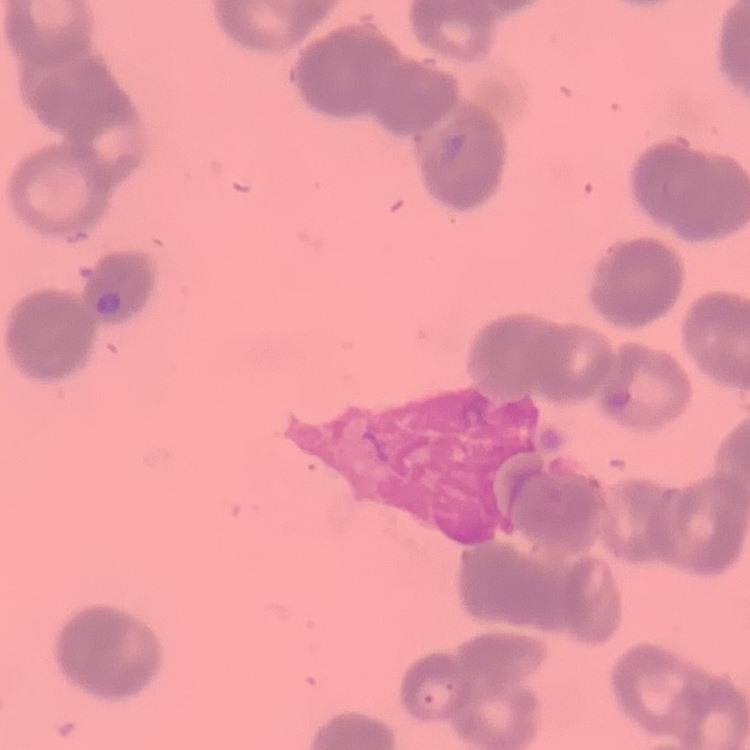
Summary:
  - Red blood cell morphology: rouleaux formation
  - Stain: Field's or Giemsa
  - Image type: one tile cut from a larger photomicrograph
  - Preparation: thin blood smear